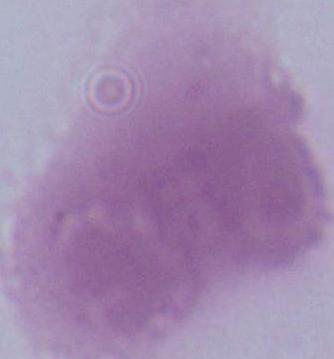
identification = erythrocyte
modality = photomicrograph
magnification = 1000x